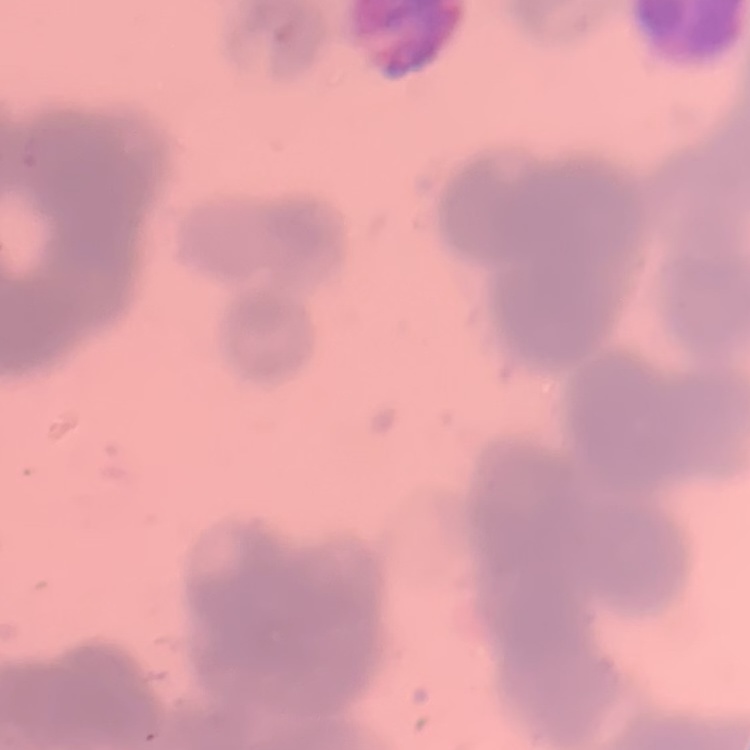 The erythrocytes exhibit rouleaux formation. One tile cut from a larger photomicrograph. Thin blood film. Field's or Giemsa stain.